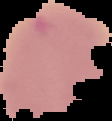

Summary:
  - Malaria status: uninfected
  - Preparation: thin blood film
  - Image type: segmented cell region on a black background
  - Image size: 112×121 pixels